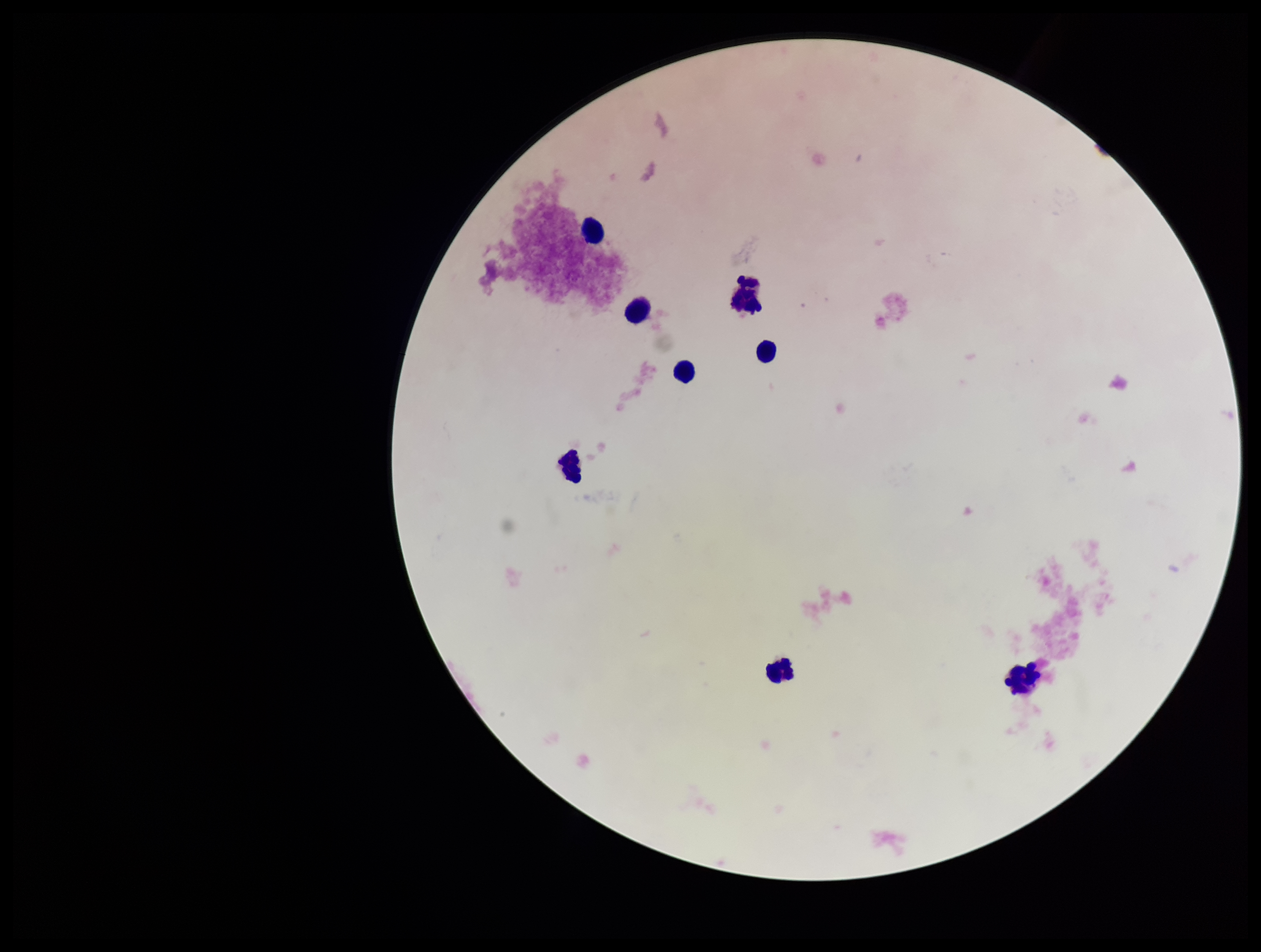

Parasite count: 0. Single field of view. Image is 1261×952 pixels. Leukocyte count: 8. Stained with Giemsa. Patient malaria status: negative. Plasmodium parasites: none detected. Preparation: thick blood smear. Photographed through the microscope eyepiece with a smartphone camera.